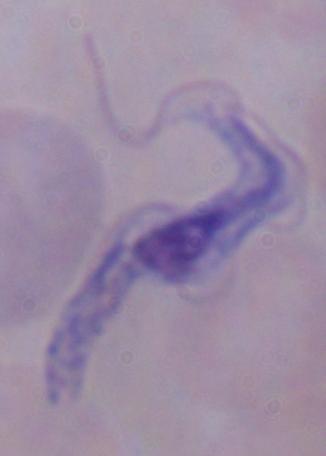
Captured at 1000x magnification. Photomicrograph. A trypanosome is shown.